Name the parasite shown.
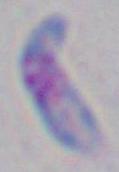

This is Toxoplasma gondii.

Summary:
  - Magnification: 1000x
  - Modality: micrograph